Assess this cell for malaria.
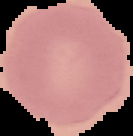
It is uninfected.

image size = 133×136 pixels
preparation = thin blood smear
image type = cell region segmented out of the field of view; surrounding area masked to black